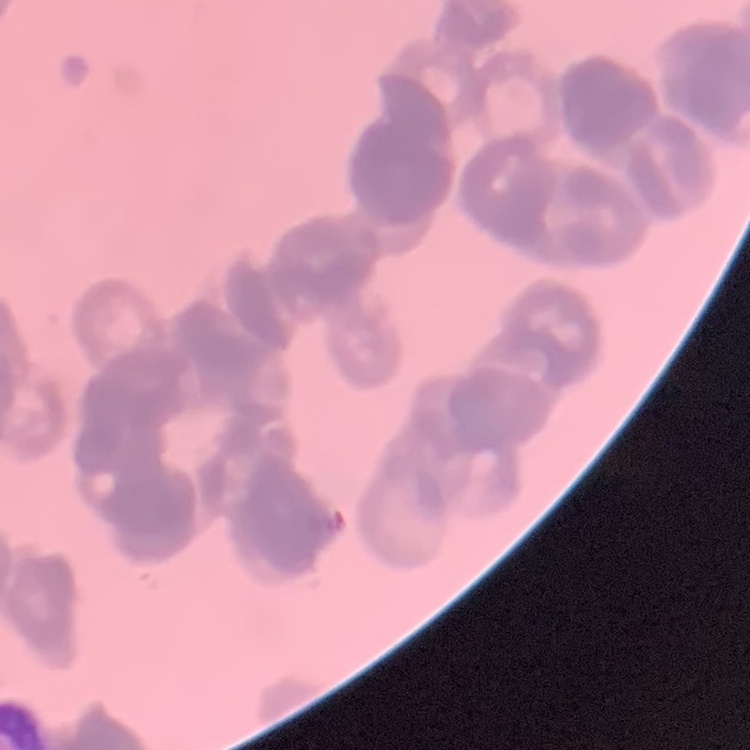

Summary:
  - Red blood cell morphology: rouleaux formation
  - Preparation: thin peripheral smear
  - Image type: one tile cut from a larger photomicrograph
  - Stain: Field's or Giemsa